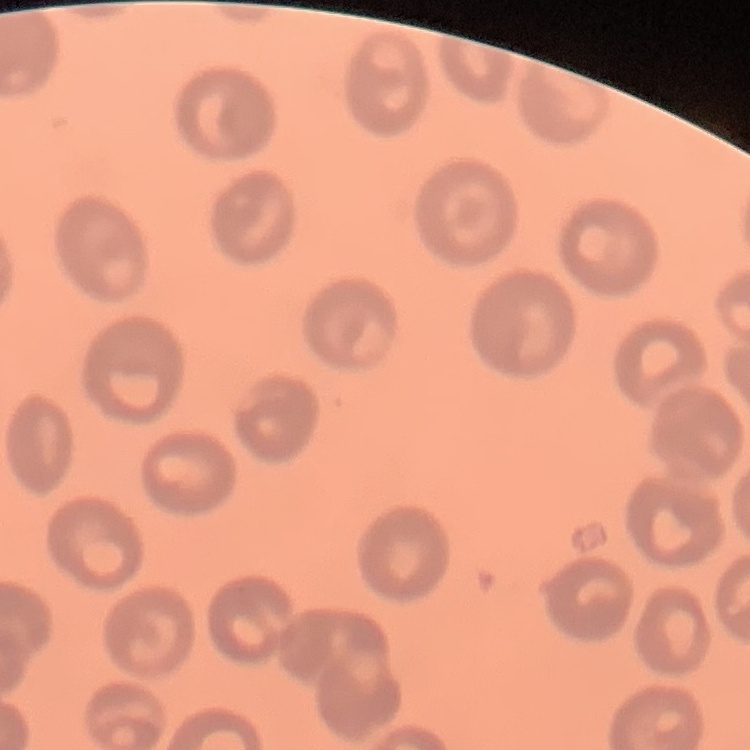

Summary:
  - Red blood cell morphology: no rouleaux formation
  - Stain: Field's or Giemsa
  - Preparation: thin peripheral smear
  - Image type: one tile cut from a larger photomicrograph